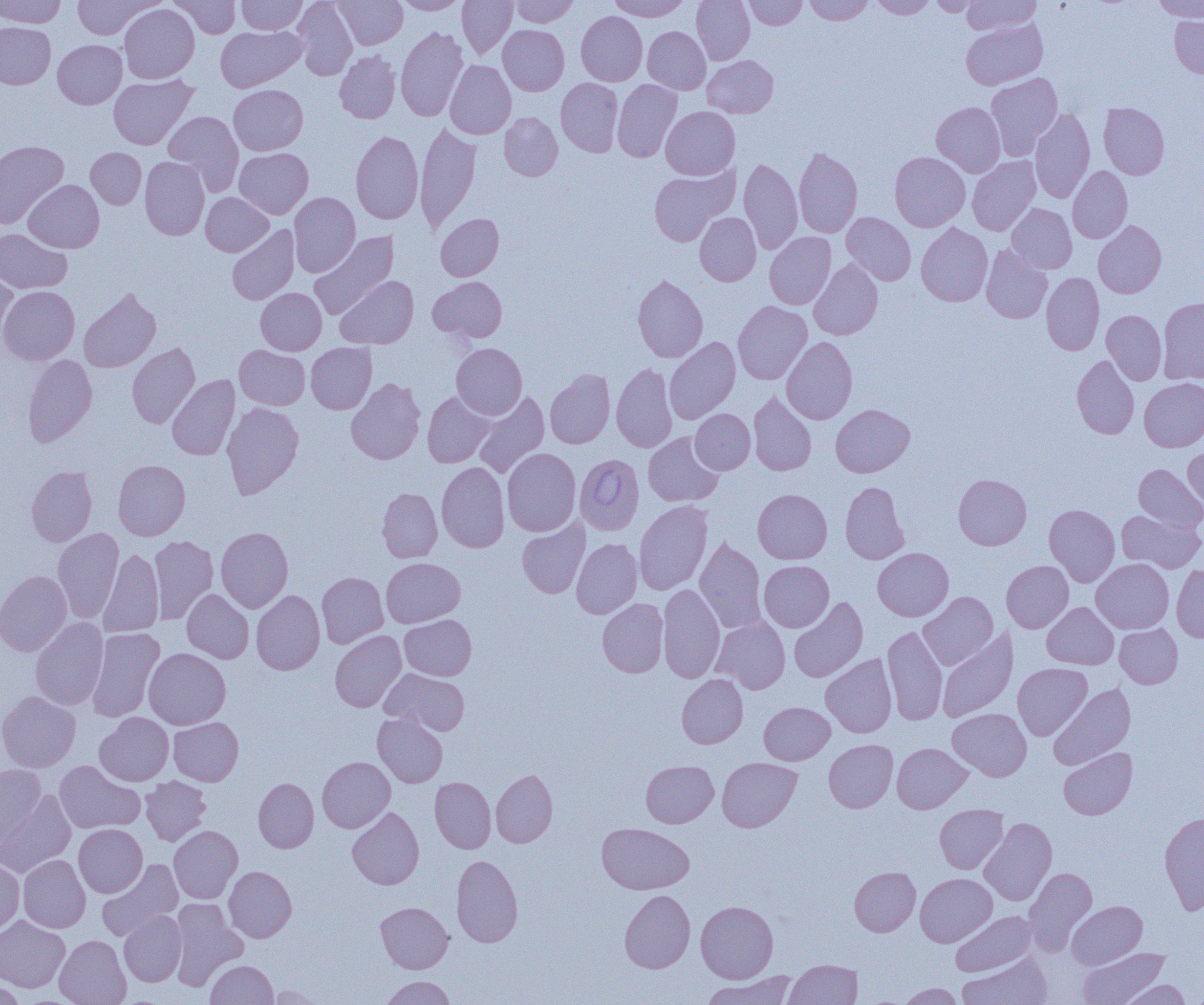

Approximate bounding boxes as (x1,y1)-(x2,y2) corner pairs in pixels. Uninfected red blood cell locations: (0,0)-(66,28), (71,0)-(161,39), (169,0)-(240,38), (237,0)-(307,34), (292,0)-(358,80), (334,0)-(407,49), (458,0)-(517,59), (510,0)-(578,27), (608,0)-(690,21), (691,0)-(754,65), (743,0)-(807,30), (804,0)-(873,25), (870,0)-(936,18), (928,0)-(983,17), (962,0)-(1041,35), (1152,0)-(1204,22), (395,1)-(468,15), (118,3)-(199,83), (576,11)-(647,86), (1169,12)-(1204,78), (961,19)-(1047,90), (0,22)-(56,89), (498,25)-(569,95), (215,26)-(306,92), (643,26)-(711,94), (396,27)-(468,121), (53,40)-(127,109), (334,50)-(400,124), (702,55)-(778,118), (445,60)-(516,139), (986,73)-(1063,160), (108,74)-(198,149), (556,78)-(623,157), (612,79)-(682,162), (229,85)-(308,155), (931,102)-(1006,177), (1098,103)-(1170,179), (661,106)-(740,180), (1029,108)-(1095,204), (163,110)-(244,193), (499,112)-(563,181), (415,121)-(481,232), (351,130)-(423,224), (0,140)-(68,229), (793,146)-(862,238), (86,148)-(146,209), (234,148)-(313,219), (890,151)-(970,232), (140,156)-(210,240), (967,156)-(1040,235), (738,158)-(802,254), (648,164)-(740,247), (1068,166)-(1132,243), (23,180)-(104,253), (201,192)-(273,256), (289,192)-(360,277), (1007,203)-(1077,273), (694,212)-(761,286), (841,212)-(916,285), (435,214)-(503,281), (1093,221)-(1166,298), (916,223)-(993,306), (227,225)-(299,305), (0,228)-(72,294), (309,231)-(399,321), (765,232)-(836,309), (981,245)-(1052,323), (809,259)-(883,340), (0,269)-(18,345), (1041,272)-(1104,355), (633,274)-(708,362), (336,276)-(418,348), (428,276)-(507,343), (0,286)-(80,365), (79,288)-(161,372), (256,288)-(326,355), (1158,296)-(1204,384), (733,301)-(812,385), (1101,310)-(1167,385), (664,337)-(740,424), (781,337)-(857,424), (128,343)-(200,428), (306,343)-(377,414), (451,343)-(527,419), (235,345)-(310,410), (23,354)-(97,447), (1071,355)-(1139,439), (611,363)-(677,453), (545,369)-(615,448), (167,375)-(240,460), (346,378)-(425,464), (1139,378)-(1204,452), (748,390)-(817,476), (472,391)-(550,478), (422,392)-(495,467), (221,402)-(304,499), (831,404)-(915,477), (690,409)-(755,474), (643,432)-(724,507), (502,448)-(581,536), (1183,448)-(1204,514), (113,460)-(190,540), (437,462)-(509,552), (1134,464)-(1204,531), (26,465)-(97,547), (953,474)-(1031,550), (840,481)-(909,564), (377,487)-(442,562), (753,489)-(832,564), (634,500)-(713,595), (1044,504)-(1120,586), (1116,510)-(1204,572), (517,518)-(590,598), (216,527)-(293,613), (53,528)-(123,623), (150,535)-(218,624), (695,537)-(766,633), (571,538)-(642,618), (98,548)-(164,637), (873,548)-(954,621), (382,558)-(465,627), (1091,558)-(1173,633), (759,560)-(834,632), (1002,560)-(1073,633), (1171,565)-(1204,643), (0,570)-(72,656), (317,572)-(388,648), (658,584)-(725,682), (182,589)-(254,663), (251,590)-(325,675), (918,592)-(998,670), (789,597)-(868,682), (597,598)-(668,677), (1042,602)-(1118,669), (400,615)-(476,680), (712,616)-(790,693), (30,617)-(108,710), (1114,624)-(1183,688), (882,625)-(948,726), (86,628)-(165,722), (937,628)-(1018,722), (330,630)-(406,712), (144,648)-(231,729), (821,654)-(897,738), (1013,663)-(1092,740), (380,668)-(470,735), (676,674)-(748,748), (1048,684)-(1136,769), (0,691)-(81,772), (759,702)-(834,765), (947,708)-(1031,781), (373,711)-(448,788), (95,712)-(173,786), (168,717)-(243,786), (824,739)-(897,812), (892,743)-(971,813), (1058,747)-(1137,819), (317,757)-(395,832), (717,758)-(802,832), (55,760)-(145,834), (641,760)-(718,828), (0,763)-(46,847), (491,769)-(557,847), (141,776)-(211,846), (430,777)-(496,853), (253,778)-(319,852), (0,789)-(76,877), (935,804)-(1008,874), (347,807)-(424,889), (1159,811)-(1204,914), (979,818)-(1057,905), (597,823)-(693,894), (73,824)-(147,897), (168,825)-(242,903), (18,854)-(91,933), (451,855)-(523,947), (0,859)-(24,935), (97,859)-(183,941), (224,866)-(297,942), (849,867)-(920,936), (1024,867)-(1097,954), (915,873)-(997,947), (619,890)-(695,973), (169,899)-(248,990), (1067,900)-(1147,969), (695,901)-(778,983), (376,902)-(453,973), (118,911)-(187,986), (951,911)-(1037,976), (0,916)-(70,993), (54,935)-(131,1005), (1079,945)-(1169,1004), (958,953)-(1052,1005), (785,959)-(861,1004), (205,960)-(277,1004), (702,971)-(799,1005), (380,975)-(456,1005), (0,979)-(25,1004), (1117,980)-(1192,1005), (896,983)-(964,1005), (265,984)-(324,1004). Babesia divergens-infected red blood cell locations: (574,454)-(644,535). Slide-level diagnosis: Babesia divergens. 1000x magnification. Thin blood smear. One field of a larger specimen. Light microscopy. Image is 1204×1005 pixels.